Report the malaria status of this cell.
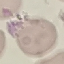
Uninfected.

Summary:
  - Image type: cell patch, automatically extracted from a larger field of view and resized to 64 × 64 pixels
  - Preparation: thin blood smear
  - Capture: smartphone through the microscope eyepiece
  - Stain: Giemsa